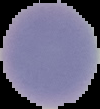
image size = 100×109 pixels
image type = segmented cell region with the area outside set to black
preparation = thin blood smear
result = no malaria parasites detected